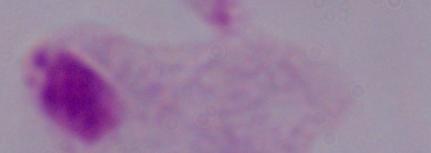

identification = trichomonad
magnification = 1000x
modality = micrograph